Report the malaria status of this cell.
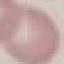
Uninfected.

capture: smartphone through the microscope eyepiece
preparation: thin blood smear
image_type: cell patch, automatically extracted from a larger field of view and resized to 64 × 64 pixels
stain: Giemsa